Name the parasite shown.
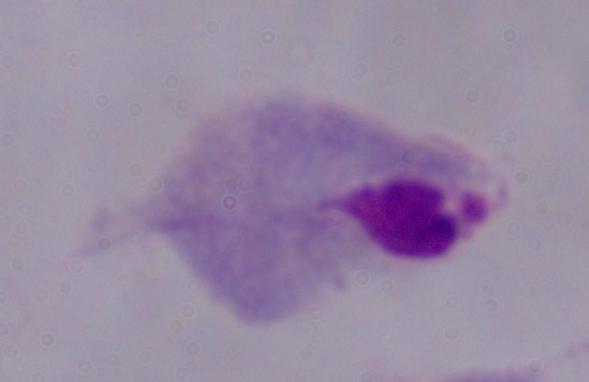

This is a trichomonad.

1000x magnification. Micrograph.